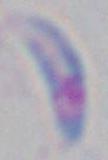

modality = micrograph
magnification = 1000x
identification = Toxoplasma gondii